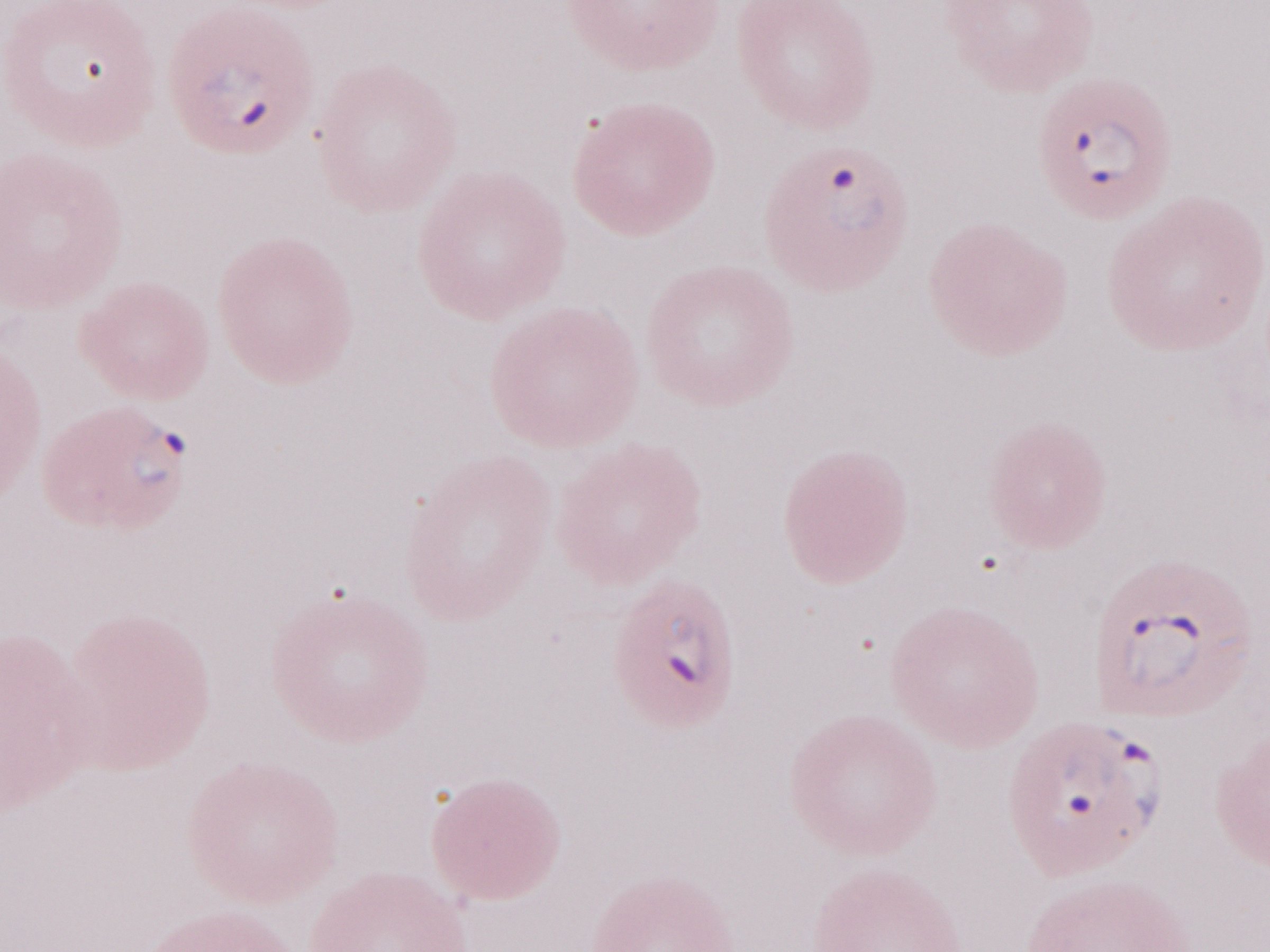

Thin blood smear. May-Grünwald-Giemsa stain. Single field of view. Magnification: 1,000x. Patient diagnosis: malaria infection. Olympus BX43 microscope and DP73 digital camera. Image is 1270×952 pixels.